Report the malaria status of this cell.
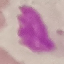

It is uninfected.

Summary:
  - Preparation: thin smear
  - Stain: Giemsa
  - Capture: smartphone camera at the microscope eyepiece
  - Image type: cell patch, automatically extracted from a larger field of view and resized to 64 × 64 pixels